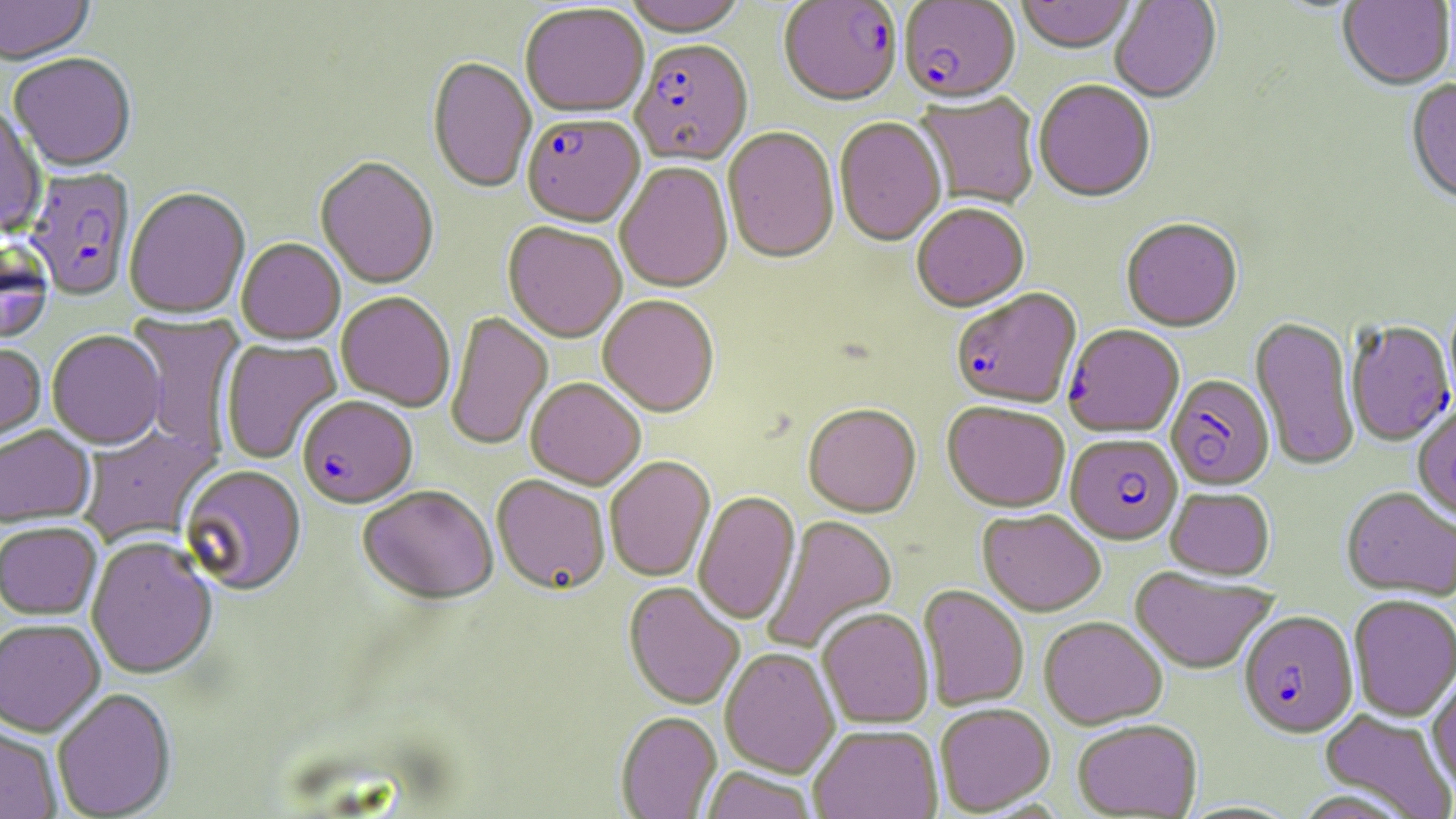 Approximate bounding boxes as named x1/y1/x2/y2 corners in pixels. Plasmodium falciparum-infected red blood cell locations: (x1=778, y1=1, x2=903, y2=109), (x1=899, y1=1, x2=1021, y2=106), (x1=630, y1=41, x2=753, y2=168), (x1=522, y1=116, x2=645, y2=230), (x1=25, y1=168, x2=136, y2=302), (x1=951, y1=290, x2=1082, y2=411), (x1=1345, y1=321, x2=1454, y2=446), (x1=1063, y1=326, x2=1184, y2=438), (x1=1165, y1=375, x2=1274, y2=490), (x1=297, y1=398, x2=417, y2=511), (x1=1065, y1=435, x2=1182, y2=545), (x1=1239, y1=611, x2=1358, y2=738). Uninfected red blood cell locations: (x1=0, y1=0, x2=95, y2=67), (x1=623, y1=0, x2=747, y2=40), (x1=1016, y1=0, x2=1134, y2=56), (x1=1110, y1=0, x2=1222, y2=105), (x1=1337, y1=0, x2=1455, y2=92), (x1=520, y1=4, x2=649, y2=121), (x1=8, y1=55, x2=136, y2=174), (x1=427, y1=59, x2=536, y2=195), (x1=1405, y1=80, x2=1456, y2=208), (x1=1034, y1=81, x2=1155, y2=205), (x1=915, y1=92, x2=1040, y2=210), (x1=0, y1=106, x2=46, y2=236), (x1=833, y1=118, x2=946, y2=248), (x1=722, y1=128, x2=840, y2=266), (x1=315, y1=158, x2=438, y2=291), (x1=615, y1=163, x2=733, y2=294), (x1=124, y1=189, x2=251, y2=320), (x1=912, y1=205, x2=1029, y2=314), (x1=1120, y1=220, x2=1243, y2=334), (x1=502, y1=224, x2=627, y2=344), (x1=0, y1=240, x2=53, y2=346), (x1=236, y1=240, x2=345, y2=346), (x1=336, y1=293, x2=455, y2=412), (x1=598, y1=297, x2=720, y2=419), (x1=127, y1=312, x2=246, y2=457), (x1=445, y1=312, x2=553, y2=451), (x1=1250, y1=317, x2=1359, y2=471), (x1=47, y1=331, x2=166, y2=451), (x1=221, y1=338, x2=342, y2=465), (x1=0, y1=343, x2=46, y2=451), (x1=526, y1=379, x2=646, y2=491), (x1=942, y1=403, x2=1070, y2=513), (x1=803, y1=405, x2=921, y2=519), (x1=1412, y1=405, x2=1456, y2=526), (x1=78, y1=424, x2=221, y2=549), (x1=0, y1=426, x2=95, y2=529), (x1=604, y1=457, x2=715, y2=583), (x1=180, y1=466, x2=307, y2=598), (x1=491, y1=477, x2=610, y2=597), (x1=358, y1=487, x2=499, y2=607), (x1=1165, y1=488, x2=1275, y2=580), (x1=1341, y1=488, x2=1456, y2=601), (x1=693, y1=492, x2=801, y2=625), (x1=978, y1=510, x2=1106, y2=617), (x1=761, y1=515, x2=898, y2=655), (x1=0, y1=523, x2=103, y2=621), (x1=86, y1=538, x2=219, y2=681), (x1=1130, y1=567, x2=1279, y2=675), (x1=623, y1=583, x2=745, y2=711), (x1=918, y1=585, x2=1029, y2=711), (x1=1348, y1=595, x2=1456, y2=723), (x1=817, y1=608, x2=934, y2=729), (x1=1038, y1=617, x2=1167, y2=729), (x1=0, y1=619, x2=105, y2=738), (x1=720, y1=648, x2=839, y2=777), (x1=1427, y1=669, x2=1456, y2=794), (x1=51, y1=690, x2=177, y2=819), (x1=934, y1=703, x2=1055, y2=816), (x1=1319, y1=709, x2=1456, y2=819), (x1=615, y1=712, x2=722, y2=819), (x1=1072, y1=719, x2=1203, y2=818), (x1=0, y1=725, x2=63, y2=819), (x1=808, y1=726, x2=942, y2=819), (x1=700, y1=768, x2=818, y2=819). Slide-level diagnosis: Plasmodium falciparum. Single field of view. Captured at 1000x magnification. May-Grünwald-Giemsa stain. Thin blood smear. Optical microscopy. Image is 1456×819 pixels.